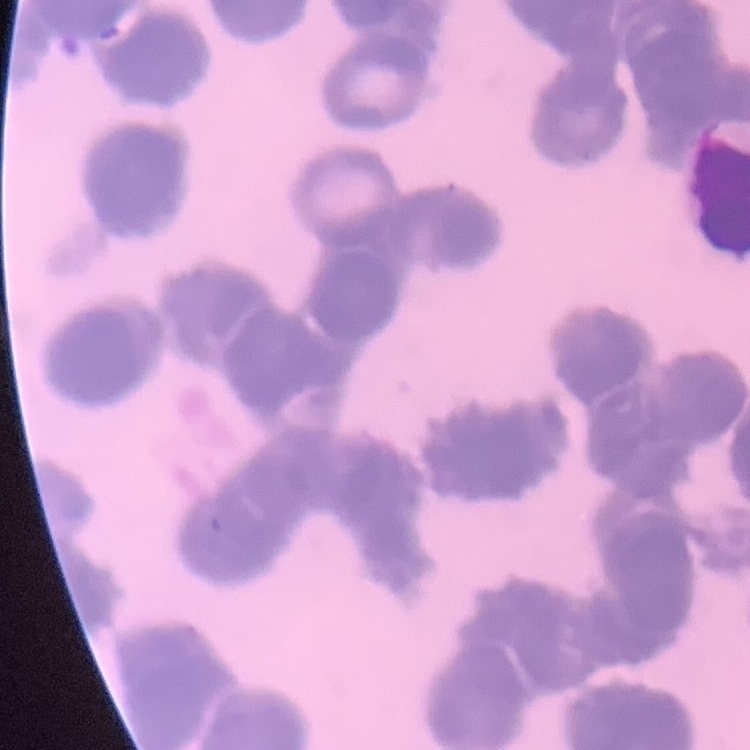
{
  "red_blood_cell_morphology": "rouleaux formation",
  "image_type": "square crop of a larger photomicrograph",
  "stain": "Field's or Giemsa",
  "preparation": "thin blood film"
}